Report the malaria status of this cell.
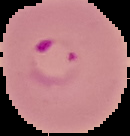
It is parasitized.

image size = 130×136 pixels
preparation = thin blood film
image type = segmented cell region with the area outside set to black